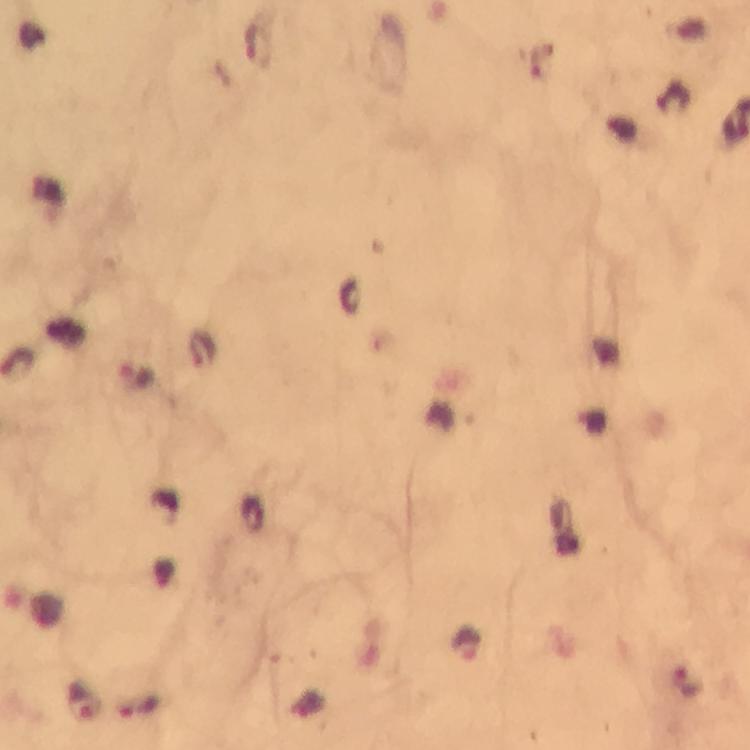
Approximate centers as {x, y} in pixels. Malaria parasite locations: {202, 348}, {137, 374}, {82, 702}, {139, 708}. Image is 750×750 pixels. From a diagnostic examination for malaria. Giemsa stain. Immersion oil applied. Smartphone photograph taken through a microscope. A crop from one field of view. At 100x magnification. Thick smear.